Identify the parasite.
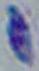
Toxoplasma gondii.

Photomicrograph. 1000x magnification.